Assess this cell for malaria.
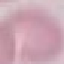

It is uninfected.

Summary:
  - Stain: Giemsa
  - Capture: smartphone through the microscope eyepiece
  - Image type: automatically extracted cell patch, resized to 64 × 64 pixels
  - Preparation: thin blood smear